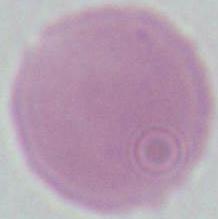
Summary:
  - Modality: photomicrograph
  - Identification: red blood cell
  - Magnification: 1000x